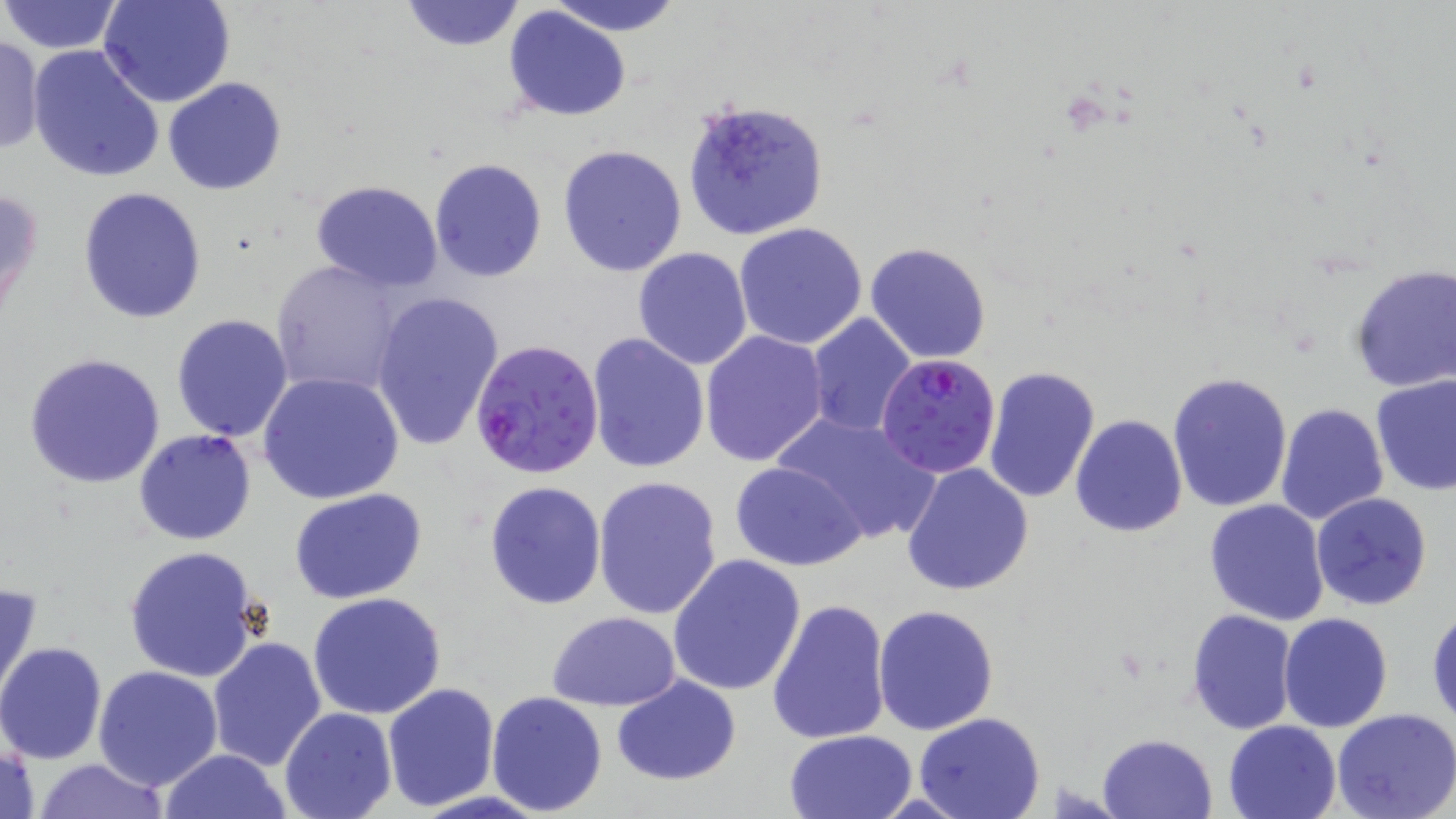
Approximate bounding boxes as [x1, y1, x2, y2] in pixels. Uninfected red blood cell locations: [0, 0, 123, 55], [99, 0, 236, 107], [399, 0, 526, 52], [543, 0, 686, 34], [504, 6, 633, 123], [0, 35, 44, 156], [28, 46, 165, 183], [163, 77, 288, 195], [680, 98, 831, 242], [557, 143, 688, 277], [428, 158, 547, 282], [299, 175, 441, 407], [310, 180, 443, 291], [1, 182, 45, 325], [77, 187, 207, 325], [734, 222, 869, 350], [865, 242, 990, 364], [632, 247, 753, 369], [269, 257, 411, 396], [1347, 263, 1456, 393], [369, 290, 505, 451], [805, 312, 917, 438], [169, 314, 293, 442], [700, 331, 830, 468], [586, 332, 709, 474], [23, 351, 168, 489], [984, 366, 1102, 505], [259, 371, 406, 505], [1168, 371, 1293, 511], [1370, 374, 1456, 495], [1275, 403, 1389, 527], [770, 411, 942, 545], [1070, 414, 1187, 539], [133, 428, 257, 547], [730, 460, 866, 570], [902, 460, 1034, 596], [593, 476, 725, 620], [483, 480, 607, 612], [290, 490, 428, 605], [1310, 492, 1433, 610], [1204, 499, 1330, 625], [122, 547, 262, 683], [666, 553, 808, 695], [1, 581, 43, 706], [308, 593, 446, 720], [768, 598, 892, 745], [873, 605, 1000, 736], [1187, 607, 1297, 733], [1429, 607, 1456, 730], [546, 612, 681, 709], [1278, 612, 1392, 732], [206, 637, 327, 772], [0, 641, 106, 764], [93, 666, 222, 791], [613, 675, 741, 785], [382, 681, 501, 811], [485, 690, 609, 816], [279, 706, 397, 819], [1332, 710, 1455, 819], [913, 713, 1045, 819], [1223, 719, 1344, 819], [783, 729, 918, 818], [1097, 733, 1219, 819], [1, 739, 41, 819], [158, 748, 293, 819], [29, 758, 172, 818]. Plasmodium falciparum-infected red blood cell locations: [469, 337, 604, 478], [875, 356, 1000, 480]. Slide-level diagnosis: Plasmodium falciparum. One field of a larger specimen. Thin blood film. Optical microscopy. Image is 1456×819 pixels. May-Grünwald-Giemsa-stained preparation. 1000x magnification.